Point out each Plasmodium parasite.
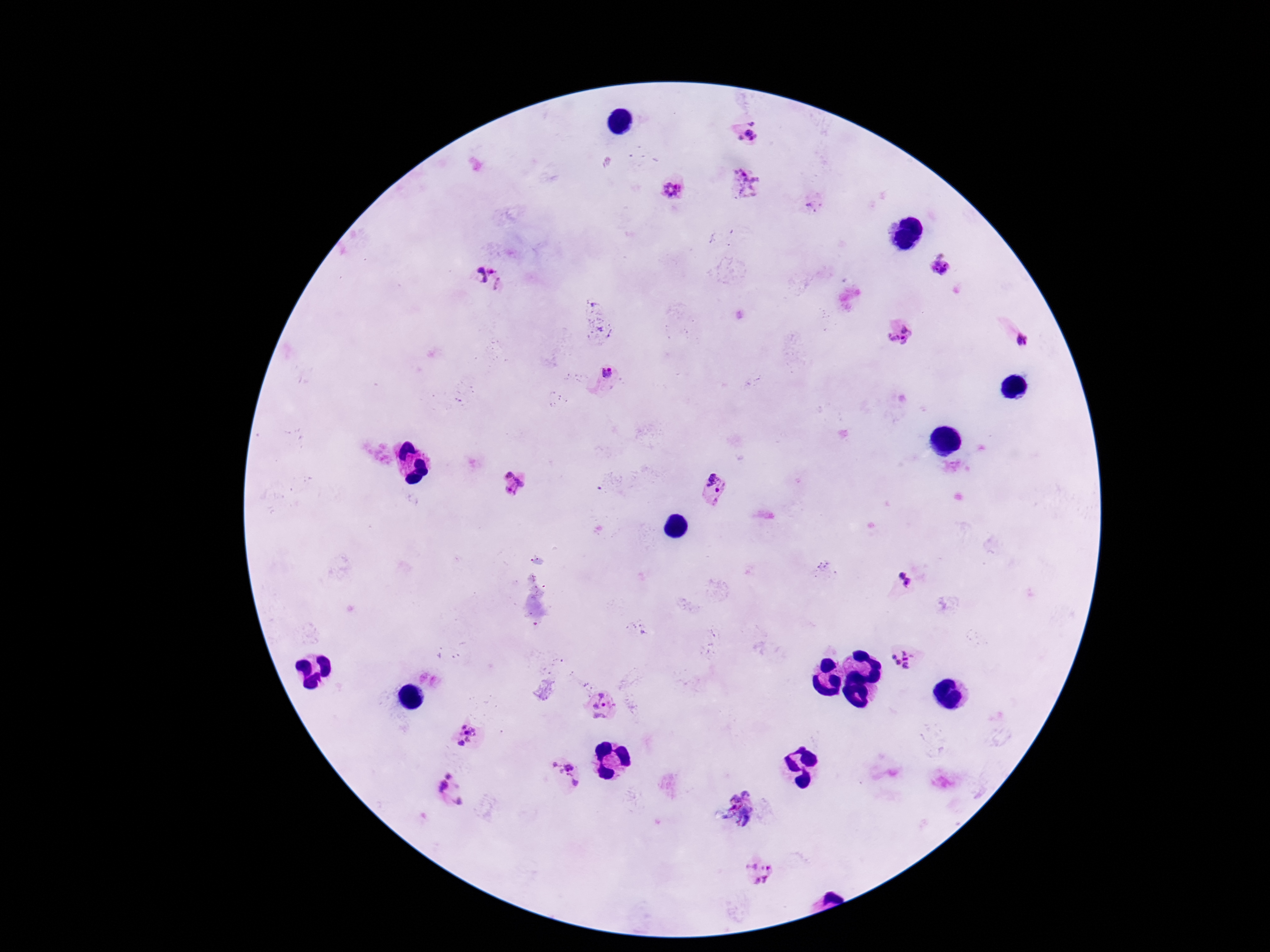
Approximate centers as {x, y} in pixels.
Plasmodium parasites: {748, 132}, {747, 185}, {670, 190}, {814, 204}, {941, 264}, {489, 278}, {900, 335}, {1022, 341}, {607, 373}, {717, 482}, {512, 483}, {901, 575}, {909, 583}, {904, 660}, {603, 705}, {465, 736}, {563, 776}, {451, 790}, {742, 805}, {763, 872}.

Summary:
  - Preparation: thick blood smear
  - Stain: Giemsa
  - Patient malaria status: positive
  - Magnification: 100x
  - Capture: smartphone camera through the microscope eyepiece
  - Image size: 1270×952 pixels
  - Field of view: single